Assess this cell for malaria.
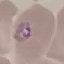
It is parasitized.

Summary:
  - Preparation: thin blood film
  - Stain: Giemsa
  - Capture: smartphone through the microscope eyepiece
  - Image type: automatically extracted cell patch, resized to 64 × 64 pixels